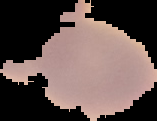 From a thin blood film. Image is 157×121 pixels. Malaria status: uninfected. The area outside the segmented cell region is set to black.